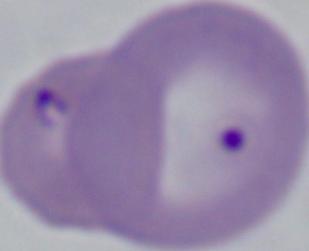 Micrograph. A Babesia parasite is seen. 1000x magnification.